Identify the cell.
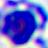

This is a leukocyte.

magnification: 400x
modality: photomicrograph